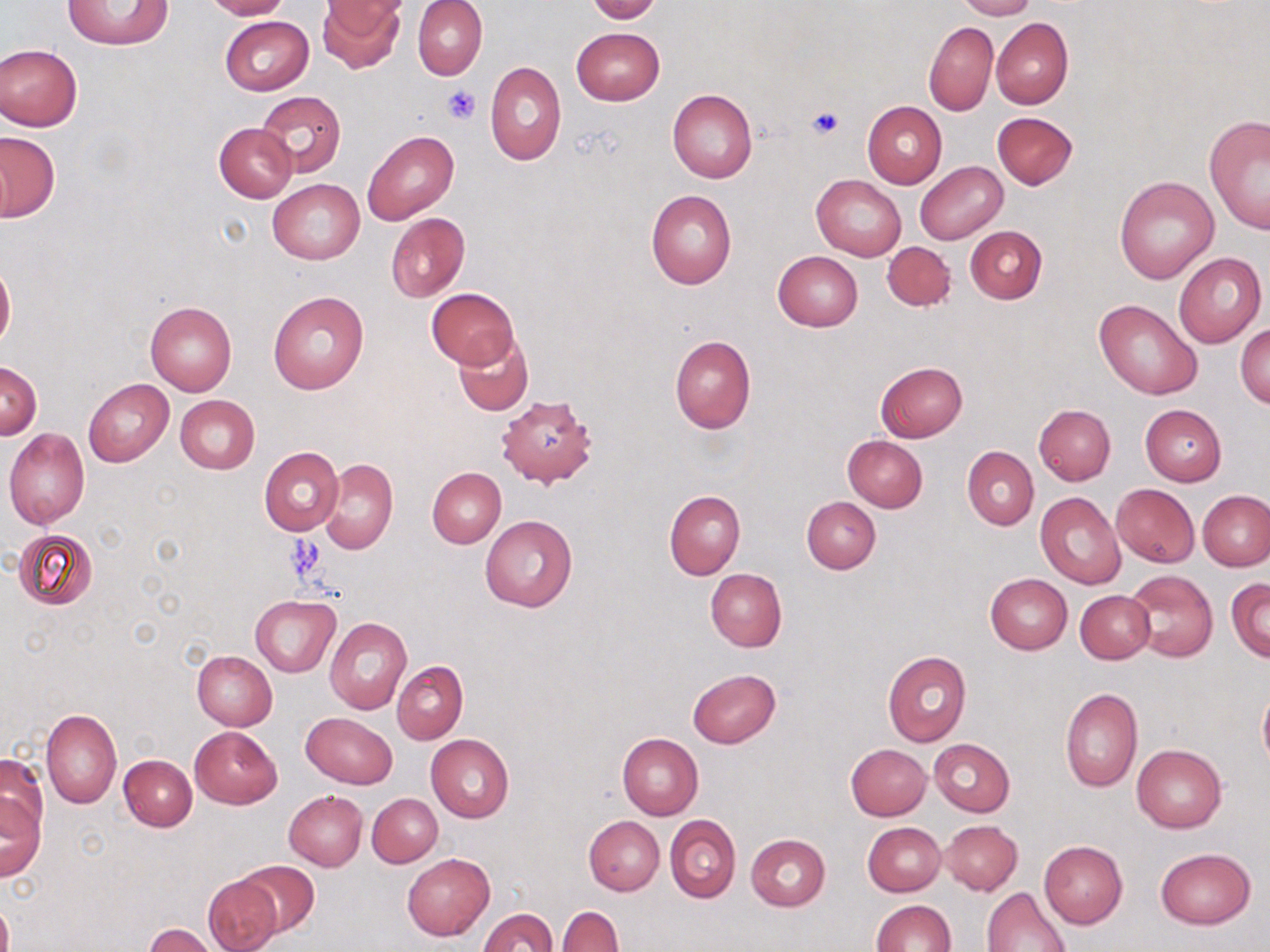

Approximate bounding boxes as (x1, y1, x2, y2) in pixels. Uninfected red blood cell locations: (63, 0, 172, 49), (203, 0, 289, 19), (317, 0, 405, 74), (326, 0, 416, 21), (414, 0, 488, 80), (586, 0, 661, 23), (956, 0, 1035, 20), (219, 16, 313, 95), (991, 18, 1073, 109), (924, 21, 998, 116), (572, 26, 664, 104), (0, 45, 83, 131), (485, 62, 566, 166), (667, 89, 757, 184), (255, 90, 345, 176), (862, 101, 947, 187), (992, 112, 1078, 189), (1204, 115, 1270, 233), (214, 122, 297, 202), (362, 129, 458, 225), (0, 131, 60, 222), (915, 161, 1007, 245), (812, 174, 907, 260), (1114, 175, 1221, 284), (268, 179, 364, 262), (646, 189, 737, 290), (386, 213, 470, 301), (965, 226, 1047, 304), (882, 241, 957, 312), (772, 250, 863, 330), (1172, 251, 1265, 347), (0, 258, 15, 350), (426, 288, 519, 370), (268, 291, 369, 394), (1094, 299, 1203, 401), (145, 302, 237, 394), (1235, 323, 1270, 407), (453, 333, 534, 417), (670, 334, 756, 434), (0, 361, 41, 439), (875, 362, 968, 442), (84, 378, 173, 468), (175, 395, 259, 473), (497, 395, 597, 489), (1033, 404, 1116, 484), (1140, 404, 1226, 487), (4, 428, 90, 529), (843, 435, 927, 511), (962, 446, 1039, 530), (259, 447, 344, 534), (320, 459, 398, 553), (427, 467, 506, 549), (1111, 483, 1200, 566), (664, 490, 745, 579), (1198, 490, 1269, 572), (1034, 492, 1124, 588), (802, 497, 881, 573), (481, 516, 577, 612), (13, 530, 99, 610), (705, 568, 786, 651), (1125, 569, 1218, 661), (984, 574, 1072, 655), (1227, 579, 1269, 661), (1074, 590, 1156, 663), (250, 595, 341, 676), (324, 617, 412, 715), (191, 651, 277, 730), (882, 651, 971, 748), (393, 661, 468, 743), (687, 668, 780, 748), (1257, 684, 1270, 776), (1060, 687, 1143, 793), (41, 708, 122, 809), (300, 713, 397, 789), (190, 726, 281, 808), (618, 732, 704, 821), (426, 734, 515, 822), (929, 738, 1015, 816), (846, 744, 931, 820), (1132, 744, 1227, 833), (119, 753, 197, 830), (0, 776, 46, 881), (283, 789, 368, 871), (368, 793, 442, 867), (584, 815, 664, 894), (666, 815, 740, 902), (940, 820, 1021, 895), (862, 821, 946, 896), (746, 834, 830, 911), (1039, 841, 1128, 928), (1155, 847, 1256, 928), (402, 852, 494, 940), (235, 859, 318, 936), (200, 873, 284, 952), (982, 887, 1071, 952), (0, 896, 13, 952), (870, 900, 956, 951), (558, 906, 624, 952), (478, 908, 557, 952), (144, 924, 217, 952). Platelet locations: (441, 84, 481, 125), (806, 106, 844, 140), (288, 535, 325, 579). Slide-level diagnosis: negative for blood parasites. May-Grünwald-Giemsa-stained preparation. Thin blood film. Optical microscopy. Single field of view. Image is 1270×952 pixels. Captured at 1000x magnification.